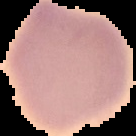
Summary:
  - Preparation: thin blood smear
  - Image size: 136×136 pixels
  - Image type: segmented cell region with the area outside set to black
  - Malaria status: uninfected